State which cell type is depicted.
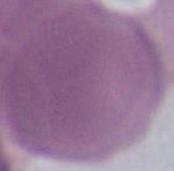
An erythrocyte.

{
  "magnification": "1000x",
  "modality": "photomicrograph"
}